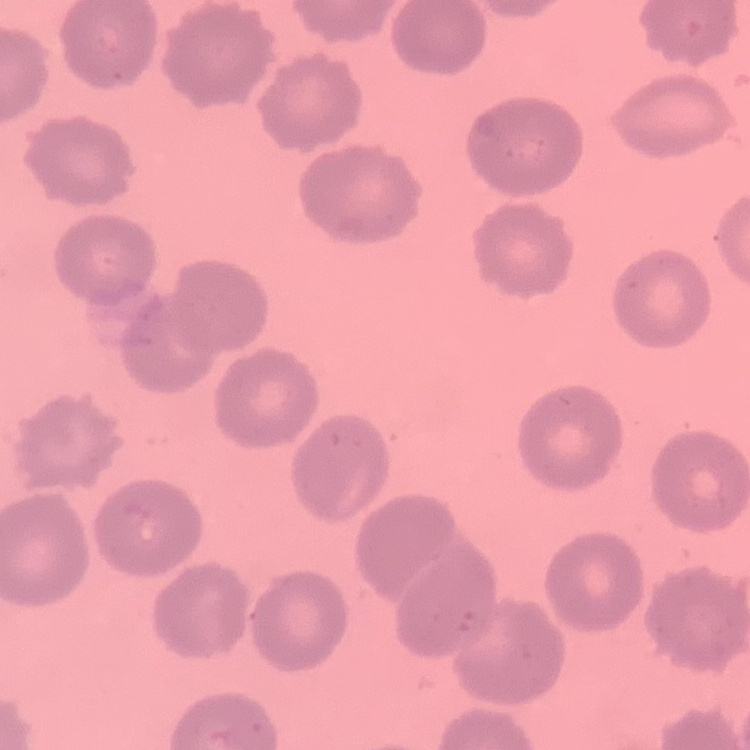

The erythrocytes show no rouleaux formation. One tile cut from a larger photomicrograph. Stained with either Field's or Giemsa. Thin blood smear.